Classify this cell by malaria status.
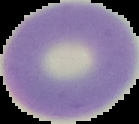

It is uninfected.

Summary:
  - Image type: cell region segmented out of the field of view; surrounding area masked to black
  - Preparation: thin blood film
  - Image size: 139×124 pixels